Report the malaria status of this cell.
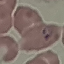
Parasitized.

capture = smartphone through the microscope eyepiece
image type = cell patch, automatically extracted from a larger field of view and resized to 64 × 64 pixels
stain = Giemsa
preparation = thin blood smear